Assess for malaria.
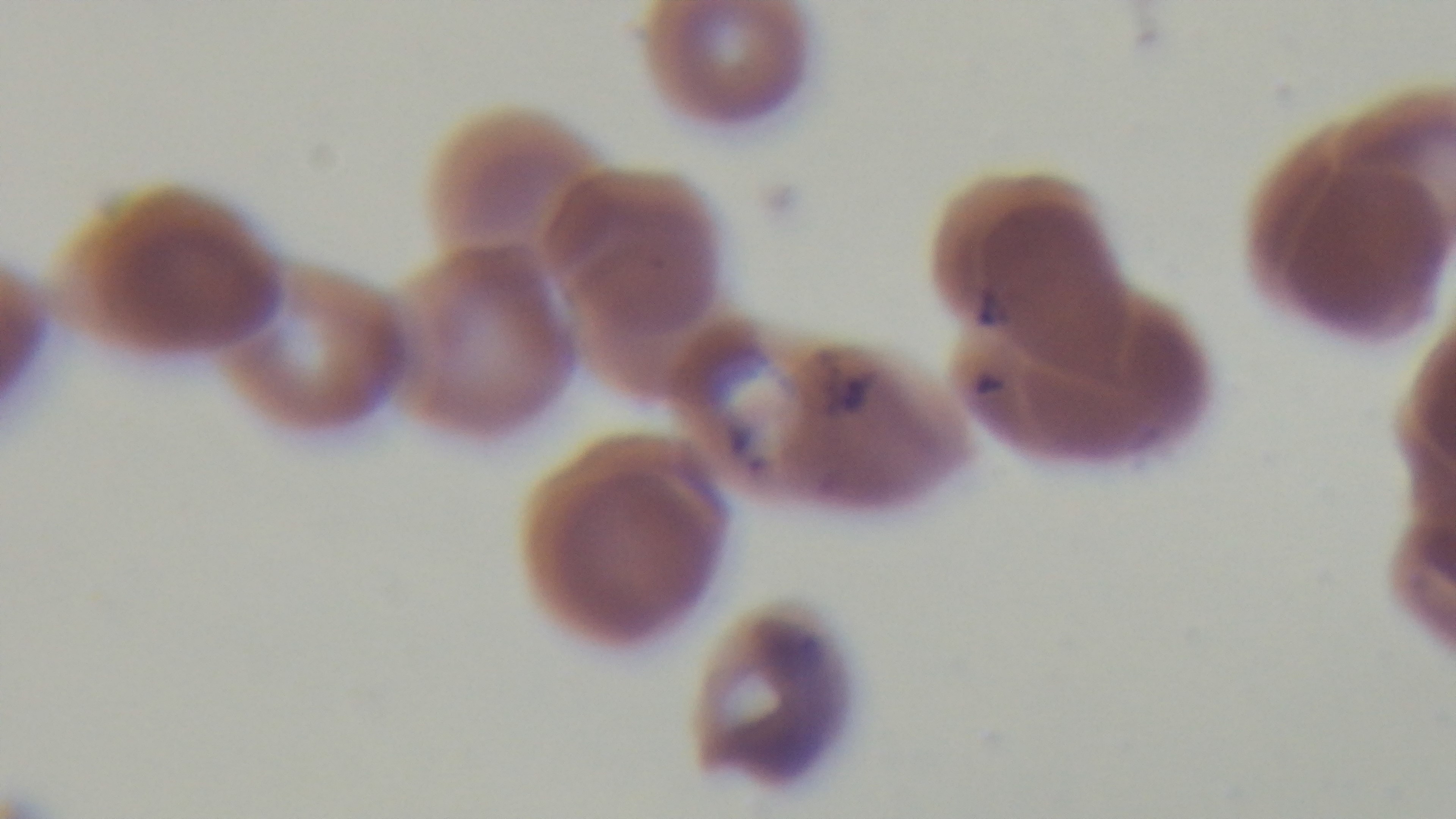

Positive.

Summary:
  - Preparation: thin smear
  - Modality: light microscopy
  - Objective: 100x oil immersion
  - Stain: Giemsa
  - Field of view: single
  - Capture: mounted 4K digital camera